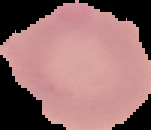
Summary:
  - Preparation: thin blood film
  - Image type: cell region segmented out of the field of view; surrounding area masked to black
  - Result: negative for malaria parasites
  - Image size: 151×130 pixels